Report the malaria status of this cell.
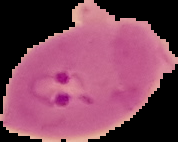
Parasitized.

From a thin blood film. Image is 178×142 pixels. The area outside the segmented cell region is set to black.